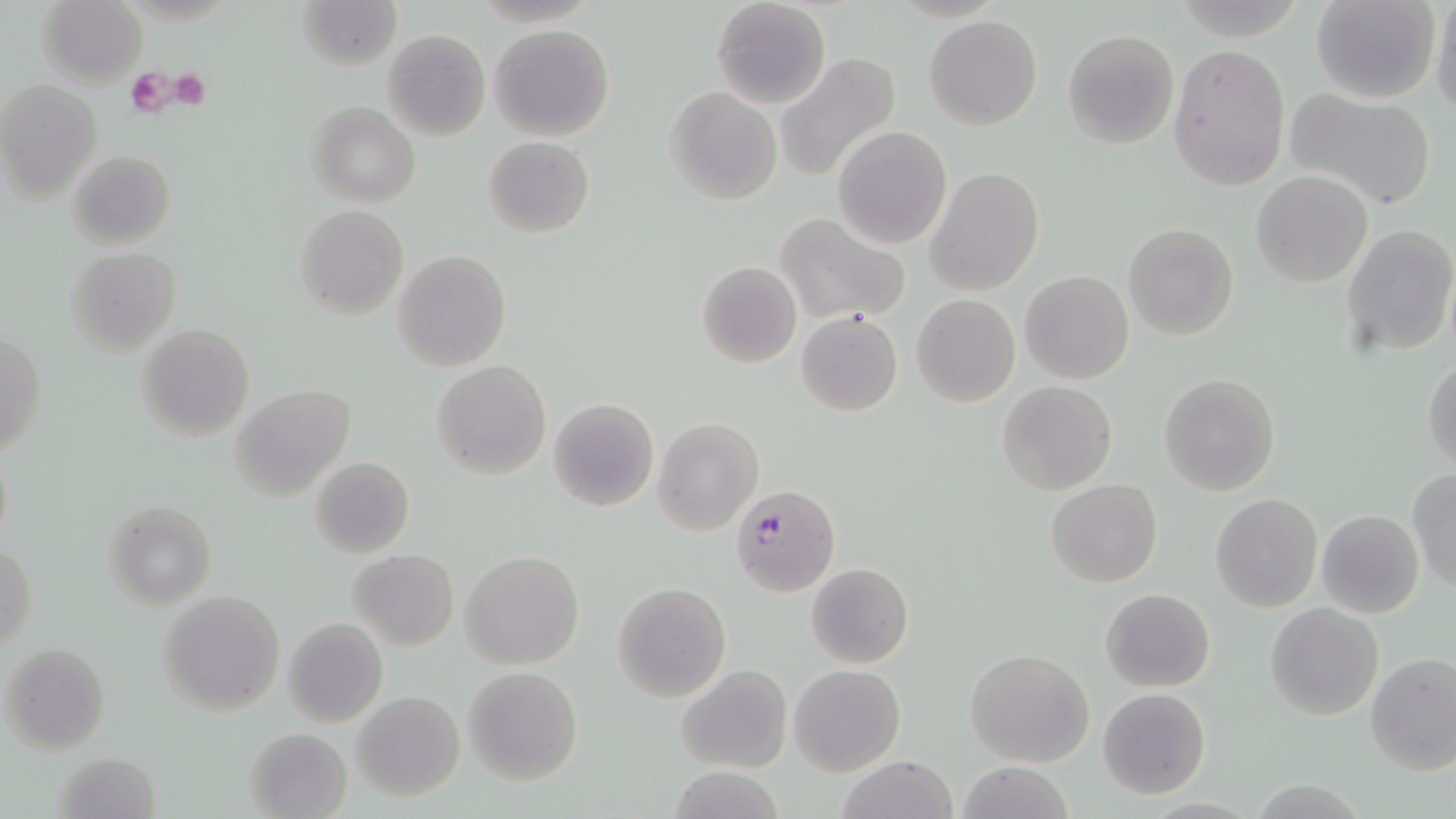
Approximate bounding boxes as [x1, y1, x2, y2] in pixels. Platelet locations: [127, 68, 174, 117], [167, 69, 211, 109]. Uninfected red blood cell locations: [297, 0, 402, 71], [709, 0, 832, 108], [1310, 0, 1442, 104], [1430, 0, 1456, 116], [38, 1, 146, 86], [923, 16, 1042, 130], [489, 24, 616, 141], [382, 28, 490, 142], [1062, 29, 1179, 148], [1167, 43, 1290, 191], [773, 52, 903, 181], [0, 80, 103, 200], [665, 87, 781, 205], [1287, 88, 1436, 210], [308, 100, 420, 205], [832, 127, 952, 249], [483, 136, 595, 238], [67, 149, 175, 250], [924, 166, 1045, 295], [1251, 171, 1372, 288], [295, 206, 408, 318], [774, 213, 911, 325], [1123, 222, 1239, 340], [1340, 224, 1454, 359], [65, 247, 180, 354], [392, 248, 511, 371], [696, 261, 802, 368], [1020, 271, 1134, 384], [912, 294, 1020, 406], [797, 308, 904, 416], [136, 324, 255, 441], [0, 334, 47, 456], [1423, 356, 1456, 473], [431, 359, 552, 481], [1159, 372, 1282, 496], [997, 381, 1117, 496], [231, 383, 358, 501], [547, 397, 660, 513], [652, 418, 765, 536], [1, 439, 14, 558], [310, 456, 414, 558], [1408, 469, 1456, 592], [1045, 479, 1163, 587], [1210, 491, 1323, 612], [102, 499, 217, 607], [1315, 509, 1425, 619], [0, 542, 37, 654], [460, 549, 584, 670], [348, 550, 459, 649], [805, 562, 915, 669], [611, 581, 732, 703], [1101, 587, 1215, 692], [158, 591, 286, 715], [1264, 604, 1383, 720], [283, 618, 387, 727], [1, 641, 111, 754], [964, 648, 1094, 768], [1365, 652, 1455, 774], [463, 664, 583, 785], [676, 664, 792, 774], [789, 664, 905, 776], [1098, 688, 1210, 798], [353, 692, 464, 801], [243, 727, 352, 819], [54, 750, 160, 819], [836, 756, 960, 818], [955, 763, 1075, 819]. Plasmodium falciparum-infected red blood cell locations: [732, 484, 840, 595]. Slide-level diagnosis: Plasmodium falciparum. May-Grünwald-Giemsa-stained preparation. Image is 1456×819 pixels. Light microscopy. Captured at 1000x magnification. Thin blood smear. One field of a larger specimen.